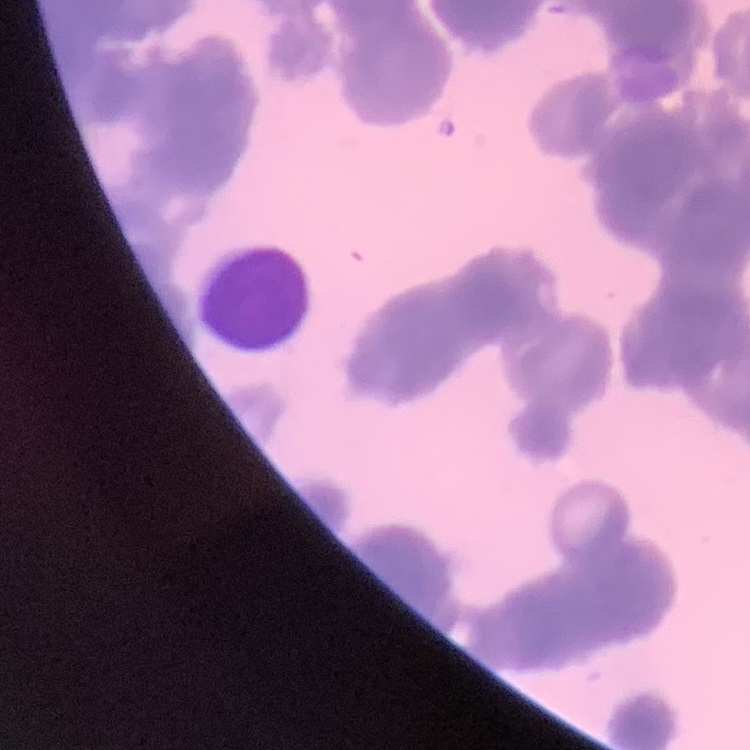

erythrocyte morphology = rouleaux formation
preparation = thin blood smear
image type = one tile cut from a larger photomicrograph
stain = Field's or Giemsa